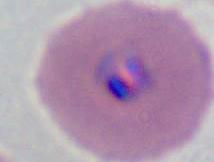
A Plasmodium parasite is shown. Captured at either 400x or 1000x magnification. Micrograph.